Point out Plasmodium parasites and leukocytes.
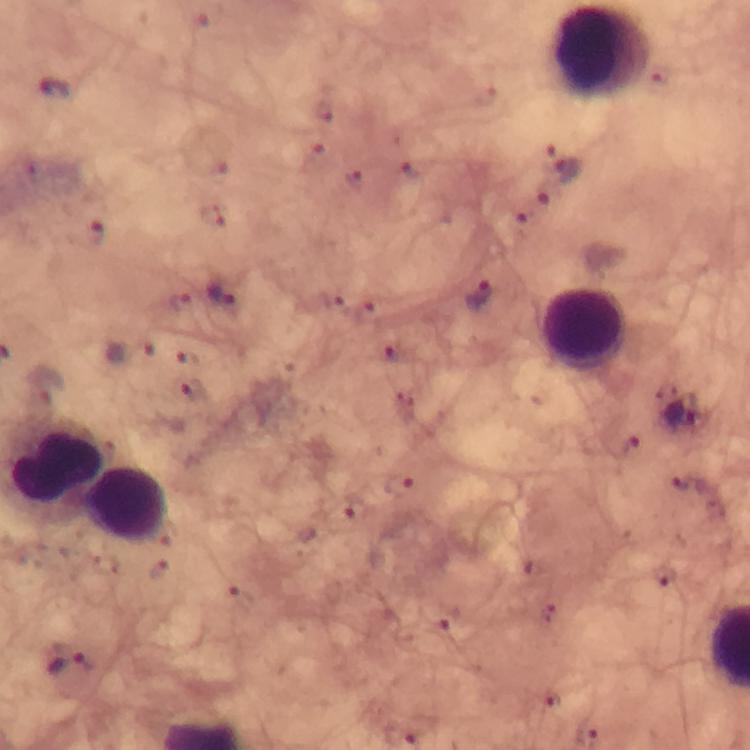

Approximate object centers, in pixels from the top-left corner.
Plasmodium parasites: (x=54, y=88), (x=571, y=171), (x=221, y=295), (x=478, y=295), (x=681, y=412), (x=72, y=673), (x=550, y=702).
Leukocytes: (x=583, y=328), (x=127, y=504).

Image is 750×750 pixels. 100x magnification. Giemsa-stained preparation. From a diagnostic examination for malaria. Immersion oil was used. Thick smear. Photographed through the microscope with a smartphone camera. A crop from one field of view.